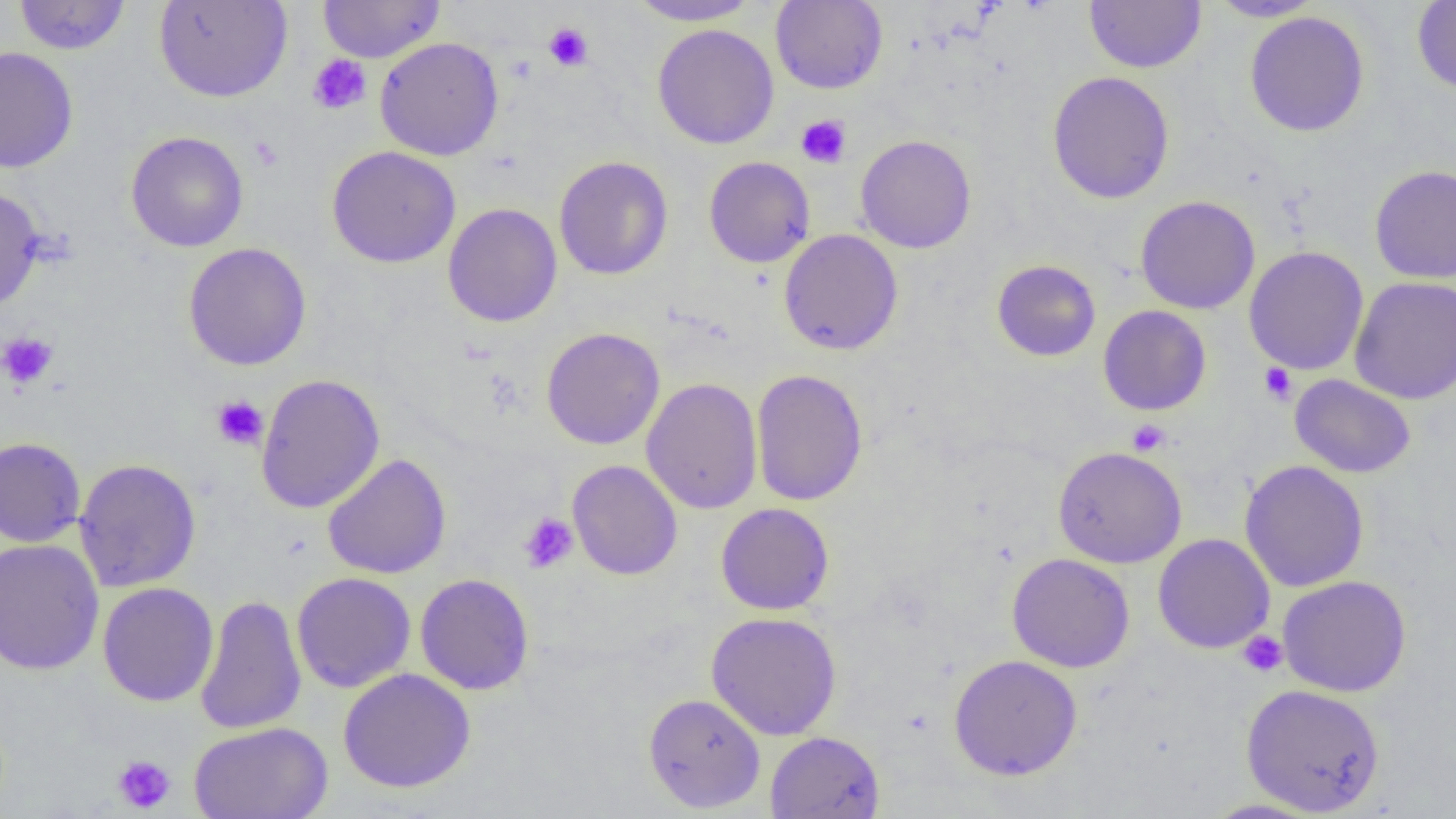 Approximate bounding boxes as (x1, y1, x2, y2) in pixels. Platelet locations: (543, 22, 593, 71), (307, 55, 371, 115), (796, 114, 852, 168), (248, 136, 283, 171), (0, 332, 59, 391), (1258, 362, 1297, 404), (211, 395, 268, 450), (1126, 419, 1171, 456), (518, 512, 579, 574), (1238, 631, 1288, 677), (112, 755, 176, 814). Uninfected red blood cell locations: (14, 0, 131, 55), (154, 0, 292, 103), (625, 0, 763, 26), (770, 0, 888, 94), (1206, 0, 1324, 21), (318, 1, 445, 63), (1085, 1, 1206, 73), (1412, 1, 1456, 96), (1245, 11, 1370, 137), (652, 23, 780, 149), (374, 37, 504, 161), (0, 47, 79, 174), (1046, 71, 1175, 204), (125, 131, 249, 252), (855, 134, 976, 254), (327, 146, 461, 268), (554, 156, 673, 280), (704, 156, 815, 268), (1369, 165, 1456, 283), (0, 186, 45, 313), (1135, 195, 1260, 314), (442, 203, 562, 327), (778, 229, 904, 356), (182, 242, 312, 371), (1243, 246, 1369, 376), (991, 259, 1101, 362), (1349, 276, 1456, 404), (1098, 305, 1211, 416), (541, 327, 665, 450), (751, 369, 868, 506), (255, 373, 385, 514), (1289, 374, 1416, 478), (641, 378, 763, 515), (0, 436, 86, 547), (1052, 446, 1187, 568), (322, 453, 452, 579), (73, 458, 202, 592), (567, 460, 683, 580), (1239, 460, 1369, 592), (715, 502, 835, 616), (1152, 533, 1275, 654), (0, 538, 104, 675), (1006, 552, 1135, 672), (291, 572, 416, 693), (415, 573, 535, 695), (1277, 575, 1412, 697), (97, 583, 219, 706), (195, 594, 307, 735), (705, 611, 842, 740), (948, 654, 1083, 780), (338, 668, 476, 793), (1241, 683, 1385, 816), (642, 692, 766, 813), (188, 721, 333, 819), (764, 731, 885, 819), (1199, 798, 1328, 818). Slide-level diagnosis: no evidence of blood parasites. Image is 1456×819 pixels. One field of a larger specimen. Optical microscopy. Captured at 1000x magnification. Thin blood smear.